Name the parasite shown.
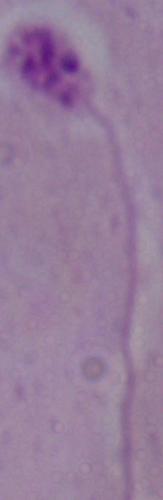
This is Leishmania.

Summary:
  - Magnification: 1000x
  - Modality: photomicrograph